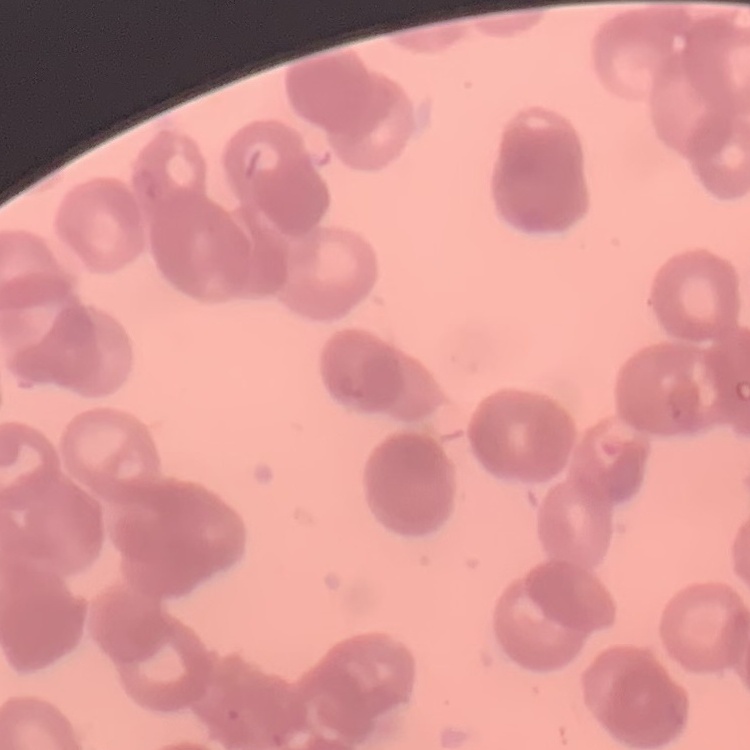

red blood cell morphology = rouleaux formation
preparation = thin blood film
image type = one tile cut from a larger photomicrograph
stain = Field's or Giemsa